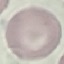

malaria_status: uninfected
preparation: thin blood smear
capture: smartphone camera at the microscope eyepiece
stain: Giemsa
image_type: automatically extracted cell patch, resized to 64 × 64 pixels